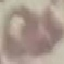
malaria_status: uninfected
stain: Giemsa
image_type: cell patch, automatically extracted from a larger field of view and resized to 64 × 64 pixels
capture: smartphone camera at the microscope eyepiece
preparation: thin blood smear